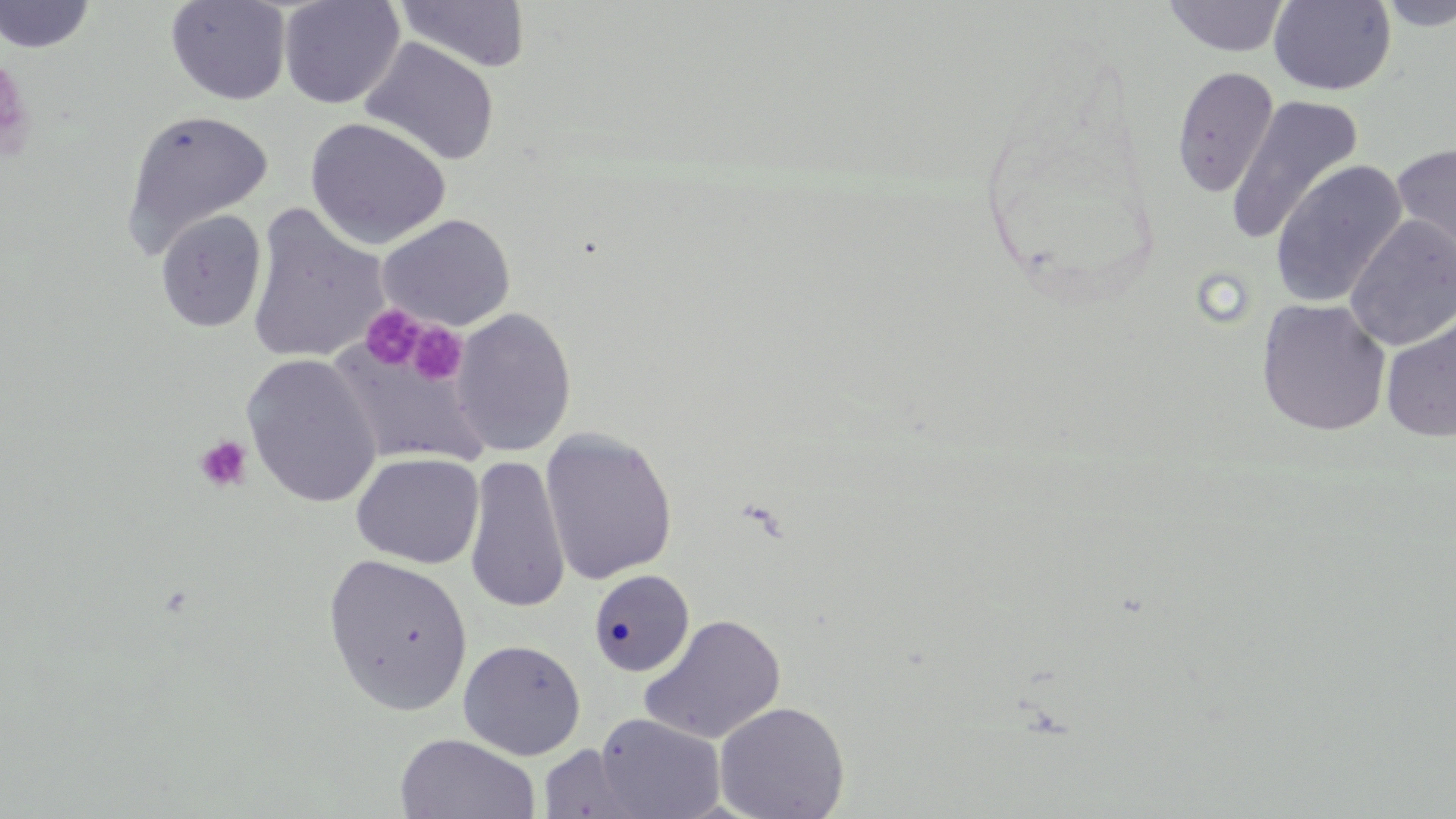
slide-level diagnosis = negative for blood parasites
platelet locations = approximate bounding boxes as [x1, y1, x2, y2] in pixels: [0, 57, 36, 162], [361, 304, 425, 369], [405, 321, 468, 386], [194, 435, 253, 493]
magnification = 1000x
field of view = one of a larger specimen
stain = May-Grünwald-Giemsa
preparation = thin blood smear
uninfected red blood cell locations = approximate bounding boxes as [x1, y1, x2, y2] in pixels: [0, 0, 96, 54], [279, 0, 405, 110], [1162, 0, 1291, 57], [1375, 0, 1456, 32], [166, 1, 291, 105], [393, 1, 530, 74], [1268, 1, 1397, 96], [360, 38, 500, 167], [1171, 67, 1279, 197], [1225, 95, 1364, 246], [121, 108, 274, 255], [305, 117, 451, 251], [1392, 140, 1456, 271], [1270, 159, 1407, 309], [246, 205, 390, 365], [155, 210, 267, 333], [378, 214, 515, 332], [1344, 215, 1456, 351], [1256, 299, 1392, 436], [451, 307, 576, 456], [1380, 311, 1456, 443], [330, 338, 490, 467], [241, 354, 382, 508], [540, 428, 678, 585], [351, 452, 484, 569], [465, 454, 570, 612], [323, 552, 474, 716], [588, 569, 695, 675], [638, 614, 787, 744], [458, 639, 586, 760], [713, 701, 850, 819], [593, 713, 726, 819], [395, 733, 541, 819], [538, 744, 651, 819]
image size = 1456×819 pixels
modality = light microscopy